State which parasite is depicted.
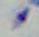

Toxoplasma gondii.

Summary:
  - Modality: photomicrograph
  - Magnification: 1000x